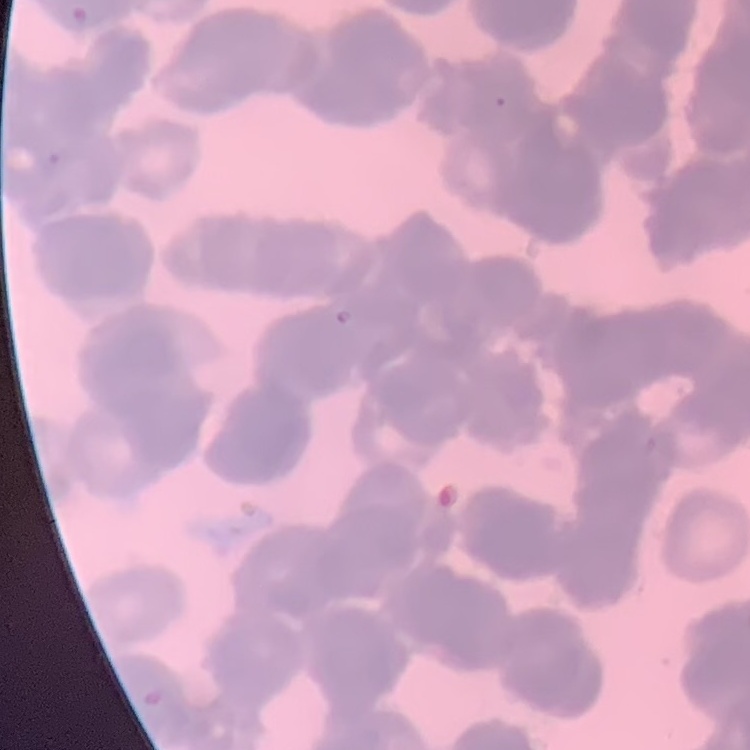
red blood cell morphology = rouleaux formation
preparation = thin peripheral smear
stain = Field's or Giemsa
image type = one tile cut from a larger photomicrograph